Give the extent of all uninfected red blood cells.
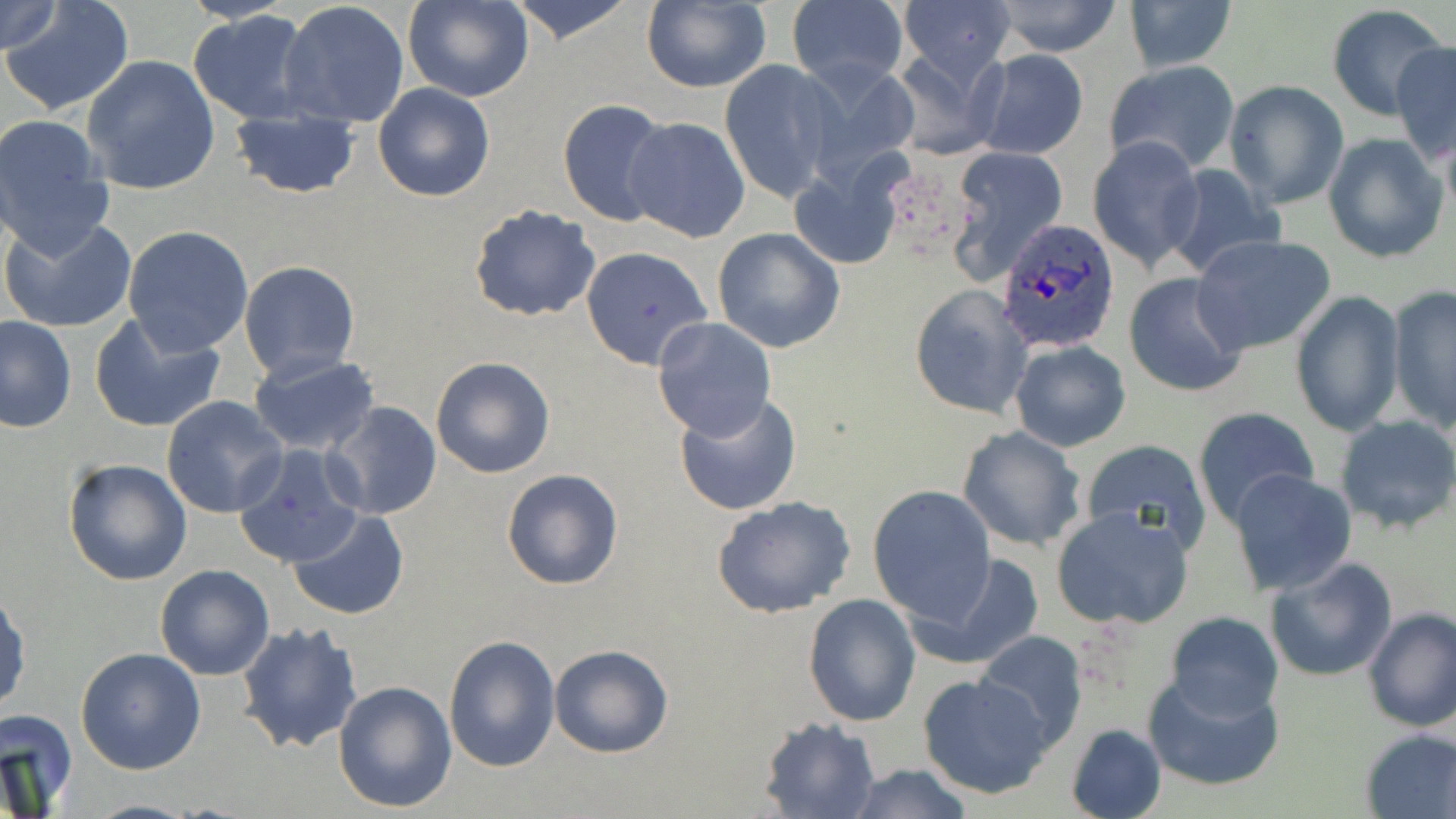

Approximate bounding boxes as [x1, y1, x2, y2] in pixels.
Uninfected red blood cells: [0, 0, 65, 55], [3, 0, 135, 116], [403, 0, 532, 102], [505, 0, 640, 47], [786, 0, 908, 92], [1123, 0, 1238, 74], [279, 1, 410, 128], [898, 1, 1013, 89], [989, 1, 1125, 57], [638, 2, 772, 92], [1325, 6, 1452, 121], [188, 10, 314, 125], [1391, 39, 1455, 163], [886, 45, 1010, 159], [972, 49, 1089, 160], [81, 55, 220, 196], [720, 58, 839, 202], [1104, 59, 1239, 174], [797, 60, 924, 190], [1225, 79, 1348, 208], [372, 83, 495, 203], [556, 99, 674, 228], [229, 108, 360, 199], [0, 114, 114, 255], [621, 116, 752, 243], [1322, 132, 1449, 264], [1089, 135, 1205, 272], [947, 148, 1070, 284], [790, 155, 909, 273], [1161, 161, 1287, 279], [468, 204, 601, 323], [2, 215, 138, 333], [123, 225, 254, 355], [711, 228, 845, 353], [1191, 235, 1337, 356], [580, 246, 713, 370], [238, 261, 361, 381], [1122, 271, 1249, 398], [909, 284, 1032, 420], [1386, 286, 1455, 432], [1290, 289, 1404, 437], [88, 311, 227, 434], [0, 316, 75, 433], [652, 317, 778, 442], [1010, 339, 1130, 452], [986, 342, 1115, 536], [248, 355, 381, 457], [430, 355, 557, 478], [673, 391, 803, 516], [161, 396, 289, 519], [325, 401, 442, 521], [1192, 407, 1320, 529], [1333, 415, 1456, 535], [262, 424, 432, 550], [956, 425, 1089, 552], [1079, 438, 1212, 554], [233, 444, 362, 568], [63, 457, 193, 585], [501, 467, 626, 590], [1228, 470, 1358, 597], [868, 485, 996, 623], [711, 495, 856, 616], [287, 508, 409, 621], [1050, 508, 1195, 631], [909, 549, 1048, 672], [1264, 556, 1398, 682], [153, 565, 274, 681], [1, 589, 29, 717], [803, 593, 923, 727], [1361, 608, 1456, 733], [1164, 611, 1284, 722], [237, 620, 363, 756], [973, 631, 1089, 749], [443, 634, 561, 773], [549, 643, 674, 758], [74, 647, 206, 774], [917, 672, 1055, 801], [1142, 672, 1285, 793], [332, 679, 457, 813], [0, 708, 77, 816], [757, 717, 878, 818], [1065, 723, 1166, 819], [1358, 727, 1456, 818], [841, 763, 977, 819], [80, 799, 203, 818].

slide_level_diagnosis: Plasmodium ovale
stain: May-Grünwald-Giemsa
magnification: 1000x
field_of_view: single
preparation: thin blood smear
modality: optical microscopy
image_size: 1456×819 pixels
plasmodium_ovale_infected_red_blood_cell_locations: 'approximate bounding boxes as [x1, y1, x2, y2] in pixels: [994, 218, 1121, 355]'